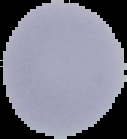

image_size: 127×139 pixels
image_type: segmented cell region with the area outside set to black
preparation: thin blood smear
malaria_status: uninfected